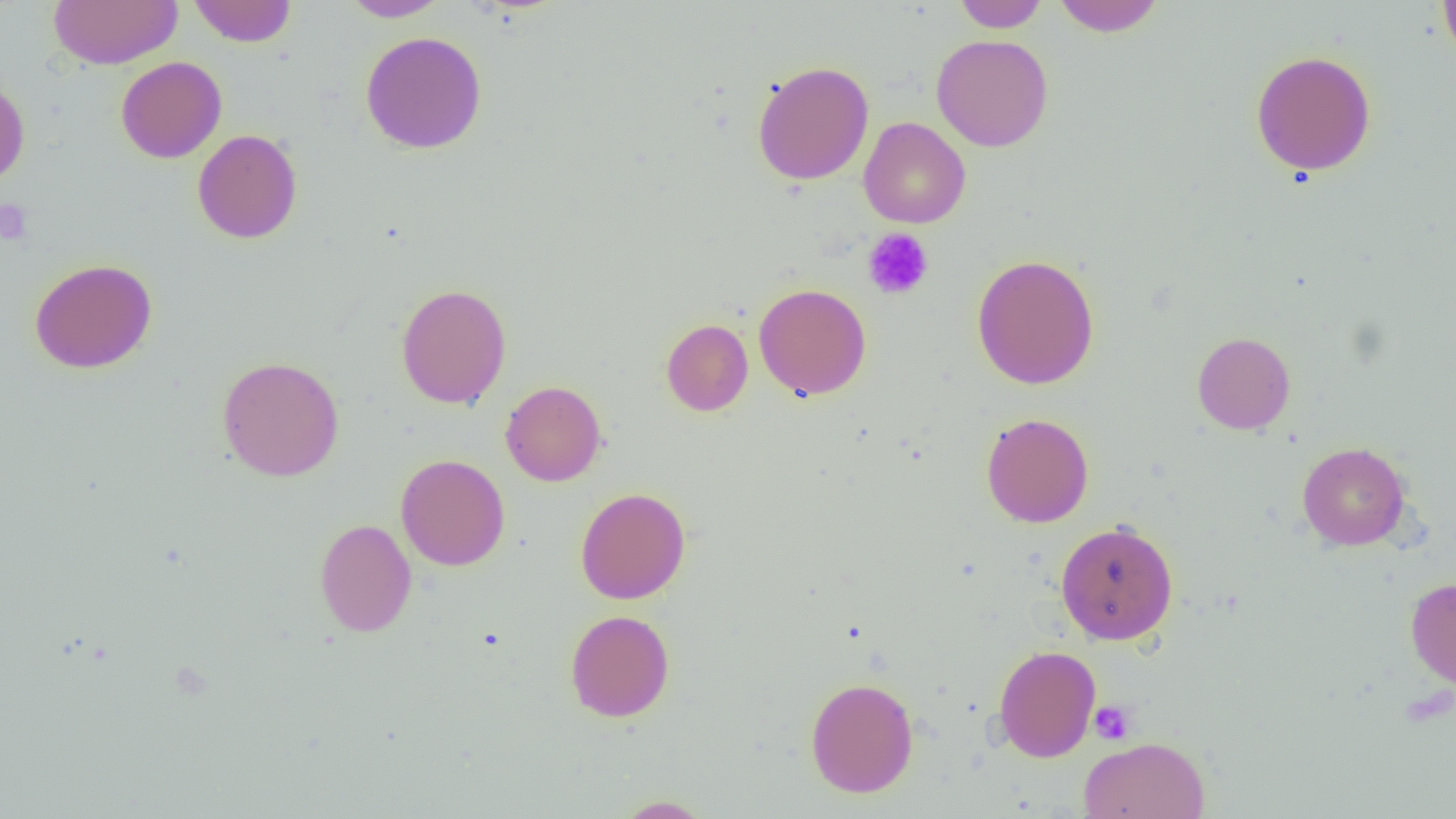
Summary:
  - Coordinate format: approximate bounding boxes as [x1, y1, x2, y2] in pixels
  - Uninfected red blood cell locations: [48, 0, 182, 69], [189, 0, 297, 47], [339, 0, 448, 21], [954, 0, 1048, 32], [1053, 0, 1165, 36], [1438, 0, 1456, 65], [360, 31, 487, 154], [931, 34, 1053, 152], [1250, 49, 1377, 177], [116, 56, 227, 163], [751, 60, 874, 185], [0, 76, 30, 187], [859, 117, 970, 229], [193, 129, 303, 244], [971, 254, 1099, 390], [29, 258, 158, 374], [396, 282, 512, 409], [753, 282, 871, 400], [661, 318, 753, 416], [1192, 331, 1295, 434], [217, 355, 344, 482], [500, 380, 606, 486], [980, 412, 1094, 528], [1297, 441, 1410, 550], [396, 454, 510, 571], [575, 486, 691, 604], [314, 518, 416, 637], [1056, 520, 1179, 645], [1405, 577, 1456, 690], [565, 609, 675, 722], [993, 645, 1101, 762], [805, 676, 919, 797], [1078, 736, 1211, 818], [613, 795, 713, 818]
  - Platelet locations: [0, 200, 33, 245], [862, 227, 934, 300], [1088, 700, 1137, 745]
  - Slide-level diagnosis: negative for blood parasites
  - Preparation: thin blood smear
  - Image size: 1456×819 pixels
  - Modality: optical microscopy
  - Field of view: one of a larger specimen
  - Magnification: 1000x